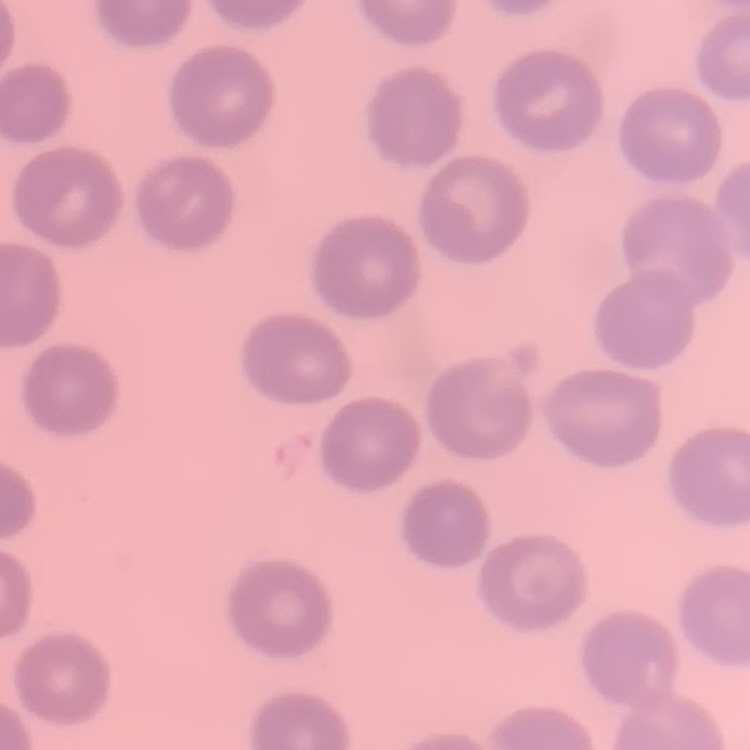

Summary:
  - Red blood cell morphology: no rouleaux formation
  - Preparation: thin peripheral smear
  - Image type: one tile cut from a larger photomicrograph
  - Stain: Field's or Giemsa